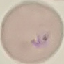 Malaria status: parasitized. Acquired by smartphone through the microscope eyepiece. Automatically extracted cell patch, resized to 64 × 64 pixels. Thin blood film. Giemsa stain.